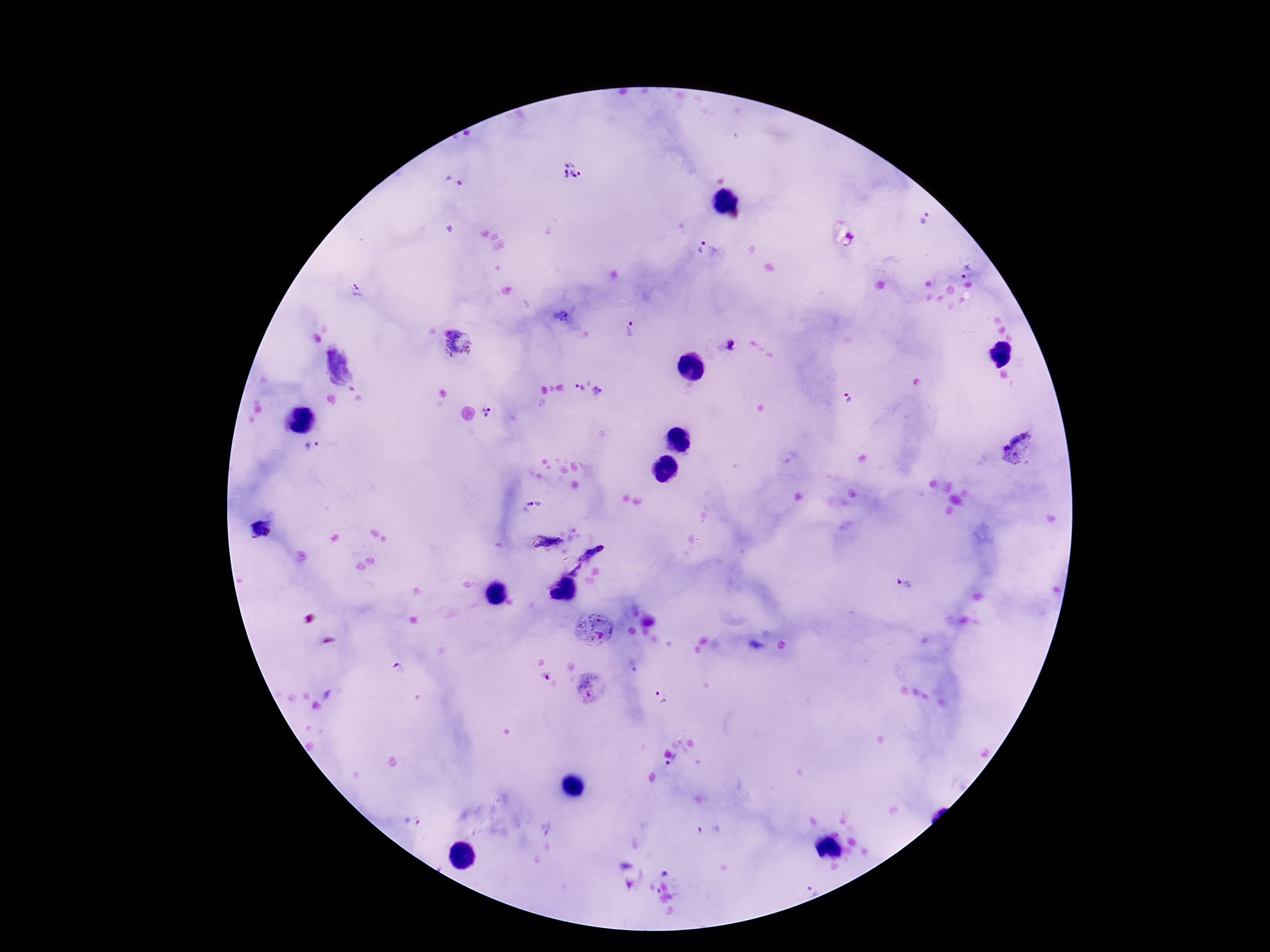

capture = smartphone camera through the microscope eyepiece
image size = 1270×952 pixels
field of view = single
preparation = thick blood smear
stain = Giemsa
Plasmodium parasite locations = approximate centers as [x, y] in pixels: [573, 172], [455, 182], [924, 218], [701, 246], [966, 270], [356, 290], [630, 329], [458, 343], [729, 345], [578, 385], [601, 391], [847, 400], [490, 412], [313, 447], [1020, 449], [534, 503], [548, 541], [593, 552], [570, 564], [904, 584], [594, 627], [398, 666], [547, 675], [591, 688], [660, 697], [675, 764]
magnification = 100x
patient malaria status = positive